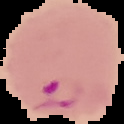
Summary:
  - Malaria status: parasitized
  - Image type: cell region segmented out of the field of view; surrounding area masked to black
  - Image size: 124×124 pixels
  - Preparation: thin blood film